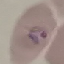

Summary:
  - Result: malaria parasites detected
  - Capture: smartphone camera at the microscope eyepiece
  - Image type: cell patch, automatically extracted from a larger field of view and resized to 64 × 64 pixels
  - Stain: Giemsa
  - Preparation: thin smear